Comment on the morphology of the erythrocytes.
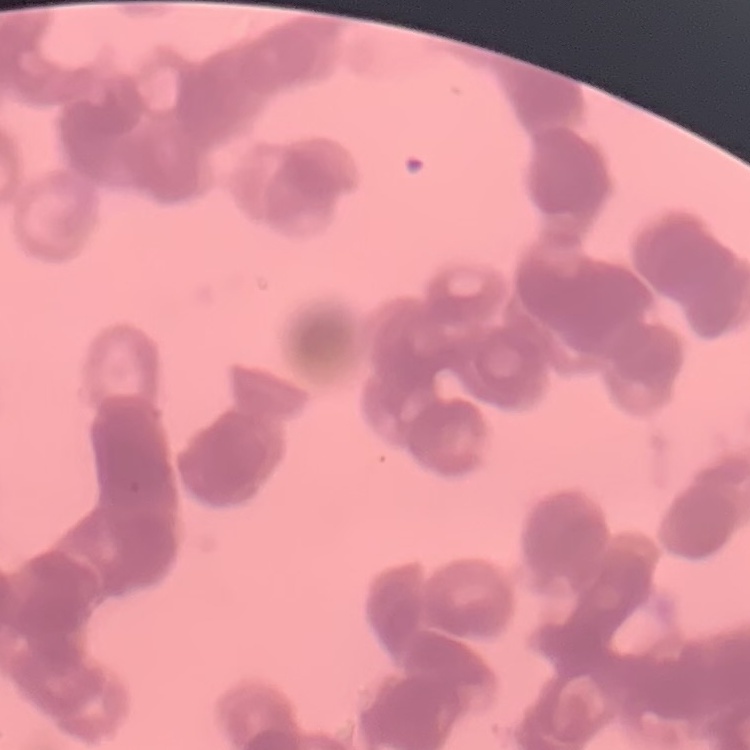

Rouleaux formation.

One tile cut from a larger photomicrograph. Thin peripheral smear. Stained with either Field's or Giemsa.